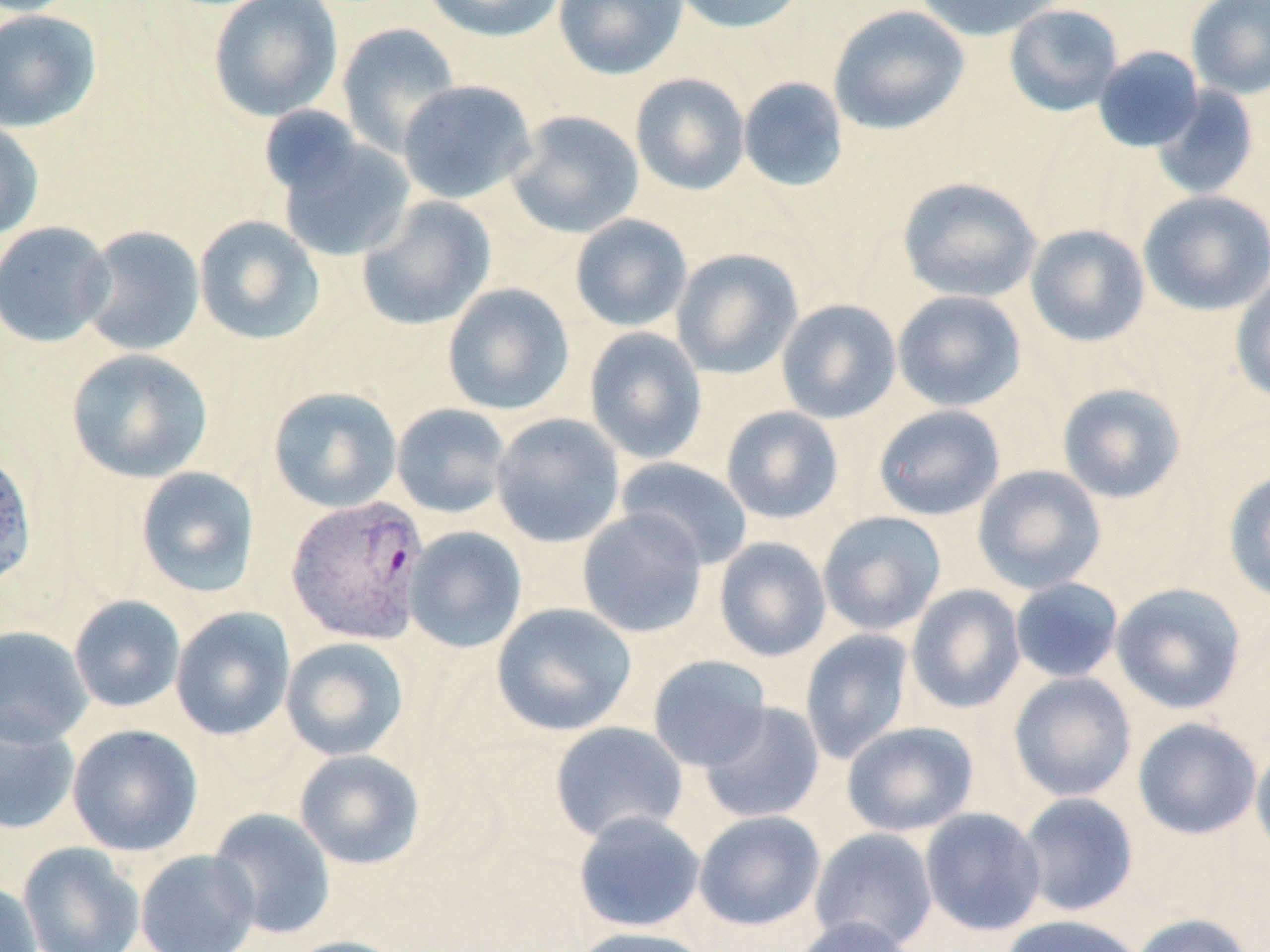

Summary:
  - Coordinate format: approximate bounding boxes as [x1, y1, x2, y2] in pixels
  - Uninfected red blood cell locations: [208, 0, 343, 122], [421, 0, 568, 43], [553, 0, 688, 80], [669, 0, 810, 34], [913, 0, 1063, 42], [1186, 0, 1270, 100], [1004, 3, 1124, 117], [828, 5, 969, 135], [0, 9, 102, 132], [336, 22, 462, 158], [1093, 46, 1205, 152], [630, 73, 750, 195], [738, 77, 849, 192], [397, 80, 537, 204], [1151, 85, 1260, 201], [258, 105, 367, 197], [506, 110, 644, 239], [0, 118, 44, 241], [273, 132, 416, 263], [897, 177, 1043, 303], [1137, 190, 1270, 316], [356, 195, 496, 331], [570, 214, 692, 332], [193, 215, 325, 346], [0, 221, 115, 348], [1024, 224, 1150, 347], [77, 225, 205, 357], [671, 248, 803, 380], [1230, 274, 1270, 406], [442, 283, 575, 416], [892, 290, 1027, 412], [776, 298, 901, 424], [584, 327, 708, 464], [65, 348, 213, 483], [1056, 382, 1186, 504], [268, 386, 403, 513], [391, 403, 512, 519], [872, 404, 1006, 521], [720, 406, 844, 524], [491, 413, 625, 548], [0, 446, 37, 591], [615, 457, 753, 570], [972, 464, 1107, 594], [135, 467, 260, 598], [1223, 468, 1270, 604], [577, 508, 708, 638], [818, 511, 946, 635], [404, 526, 527, 654], [714, 537, 832, 662], [1009, 578, 1124, 683], [1110, 582, 1247, 714], [906, 584, 1026, 714], [68, 595, 186, 712], [491, 602, 637, 737], [170, 607, 295, 740], [0, 626, 93, 747], [800, 629, 915, 764], [280, 637, 410, 761], [648, 654, 772, 771], [1007, 672, 1137, 802], [698, 702, 825, 824], [0, 712, 80, 836], [1132, 717, 1262, 840], [550, 721, 688, 843], [841, 721, 979, 837], [67, 723, 203, 856], [1250, 738, 1270, 862], [294, 749, 425, 870], [1018, 792, 1138, 917], [919, 807, 1047, 936], [208, 808, 336, 939], [573, 810, 705, 933], [693, 810, 826, 930], [809, 827, 939, 951], [17, 842, 145, 952], [135, 848, 260, 952], [0, 880, 43, 952], [1131, 913, 1254, 952], [1000, 914, 1145, 952], [791, 916, 915, 952], [569, 926, 714, 952], [280, 935, 411, 952]
  - Plasmodium vivax-infected red blood cell locations: [285, 494, 430, 645]
  - Slide-level diagnosis: Plasmodium vivax
  - Field of view: one of a larger specimen
  - Modality: light microscopy
  - Preparation: thin blood film
  - Stain: May-Grünwald-Giemsa
  - Magnification: 1000x
  - Image size: 1270×952 pixels